Locate every blood parasite and identify its species.
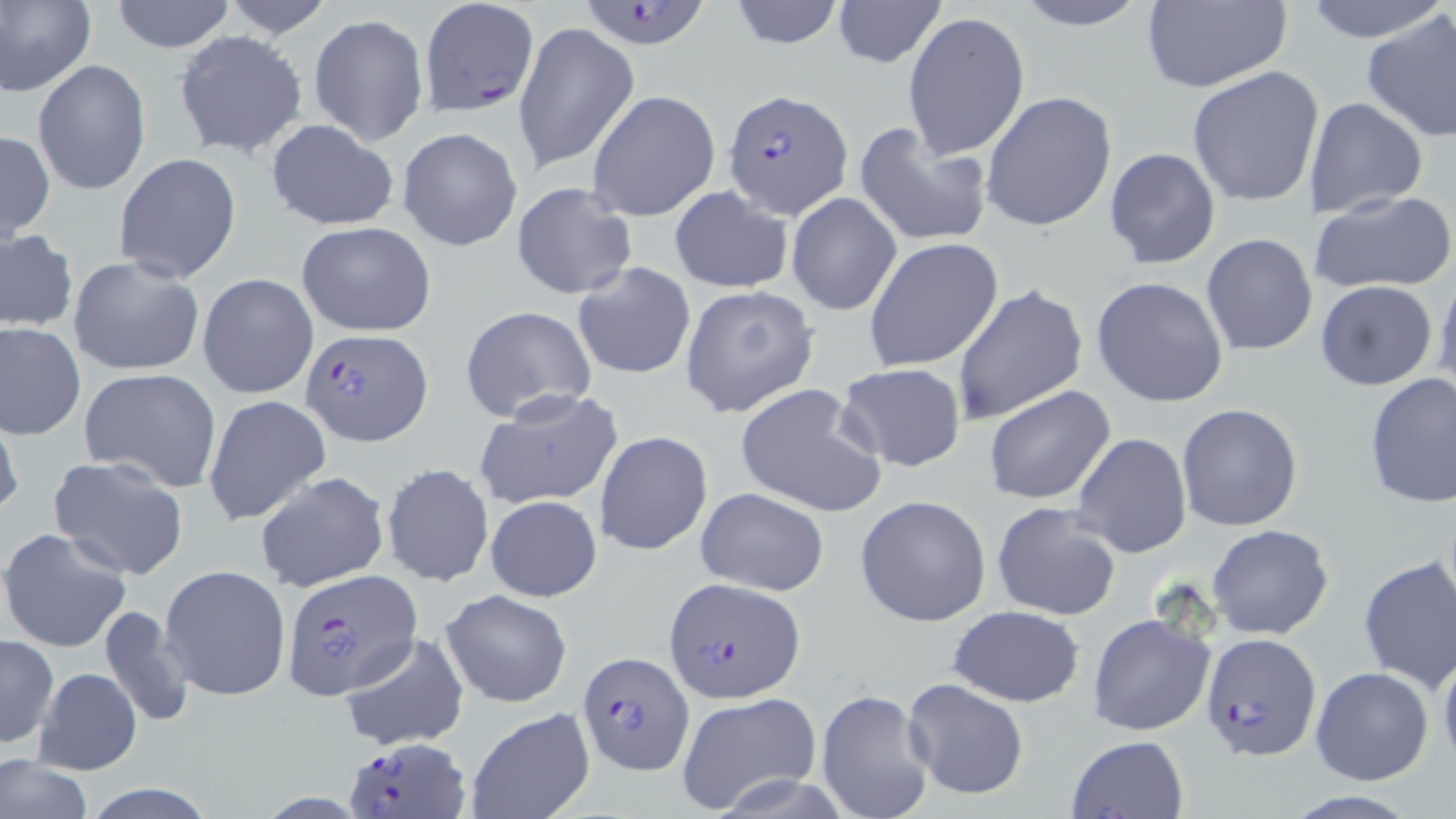

Approximate bounding boxes as [x1, y1, x2, y2] in pixels.
Plasmodium falciparum-infected red blood cells (subset): [417, 1, 538, 118], [573, 1, 718, 50], [722, 88, 855, 220], [302, 326, 432, 444], [278, 573, 421, 703], [665, 575, 807, 702], [578, 650, 694, 773], [346, 737, 470, 818].
No Plasmodium ovale, Plasmodium malariae, Plasmodium vivax, Babesia divergens, or Trypanosoma brucei observed.

Summary:
  - Uninfected red blood cell locations (subset): [0, 0, 96, 98], [110, 0, 236, 53], [220, 0, 333, 39], [726, 0, 845, 49], [831, 0, 945, 68], [1012, 0, 1155, 31], [1304, 0, 1437, 43], [1138, 1, 1293, 92], [1360, 8, 1456, 145], [903, 10, 1031, 161], [309, 14, 428, 146], [512, 21, 639, 175], [173, 30, 308, 159], [33, 60, 152, 196], [1187, 66, 1324, 208], [585, 90, 722, 222], [980, 91, 1117, 233], [1304, 96, 1427, 218], [266, 119, 399, 232], [851, 120, 992, 248], [397, 128, 522, 250], [0, 129, 54, 242], [1104, 146, 1220, 269], [113, 152, 242, 285], [511, 181, 638, 301], [668, 185, 794, 294], [1308, 189, 1456, 295], [787, 191, 900, 314], [295, 220, 436, 337], [0, 229, 77, 334], [1201, 232, 1319, 356], [864, 237, 1005, 372], [68, 254, 205, 378], [573, 262, 696, 380], [1434, 269, 1456, 402], [198, 273, 319, 397], [1091, 276, 1230, 409], [1314, 281, 1438, 391], [951, 282, 1089, 427], [679, 285, 819, 417], [460, 306, 598, 425], [1, 322, 86, 440], [835, 362, 968, 472], [80, 368, 223, 493], [1363, 371, 1455, 508], [734, 383, 887, 519], [983, 385, 1115, 505], [475, 388, 623, 510], [203, 395, 330, 526], [1176, 403, 1304, 532], [0, 408, 23, 522], [594, 430, 713, 556], [1072, 432, 1191, 559], [47, 456, 189, 580], [381, 462, 494, 587], [255, 471, 390, 593], [695, 487, 830, 596], [854, 494, 991, 627], [484, 495, 603, 602], [991, 501, 1125, 621], [1206, 526, 1333, 641], [1, 527, 132, 652], [1357, 556, 1456, 690], [160, 563, 291, 702], [439, 588, 572, 707], [98, 605, 194, 727], [947, 606, 1086, 707], [345, 611, 548, 732], [1087, 611, 1217, 738], [337, 632, 469, 752], [0, 634, 58, 748], [1437, 649, 1456, 773], [34, 667, 141, 775], [1310, 667, 1434, 785], [903, 677, 1029, 799], [814, 686, 936, 819], [675, 692, 822, 815], [465, 709, 594, 819], [1066, 735, 1188, 819], [0, 755, 94, 819]
  - Slide-level diagnosis: Plasmodium falciparum
  - Magnification: 1000x
  - Field of view: single
  - Preparation: thin blood film
  - Modality: light microscopy
  - Image size: 1456×819 pixels
  - Stain: May-Grünwald-Giemsa